Give the extent of all uninfected red blood cells.
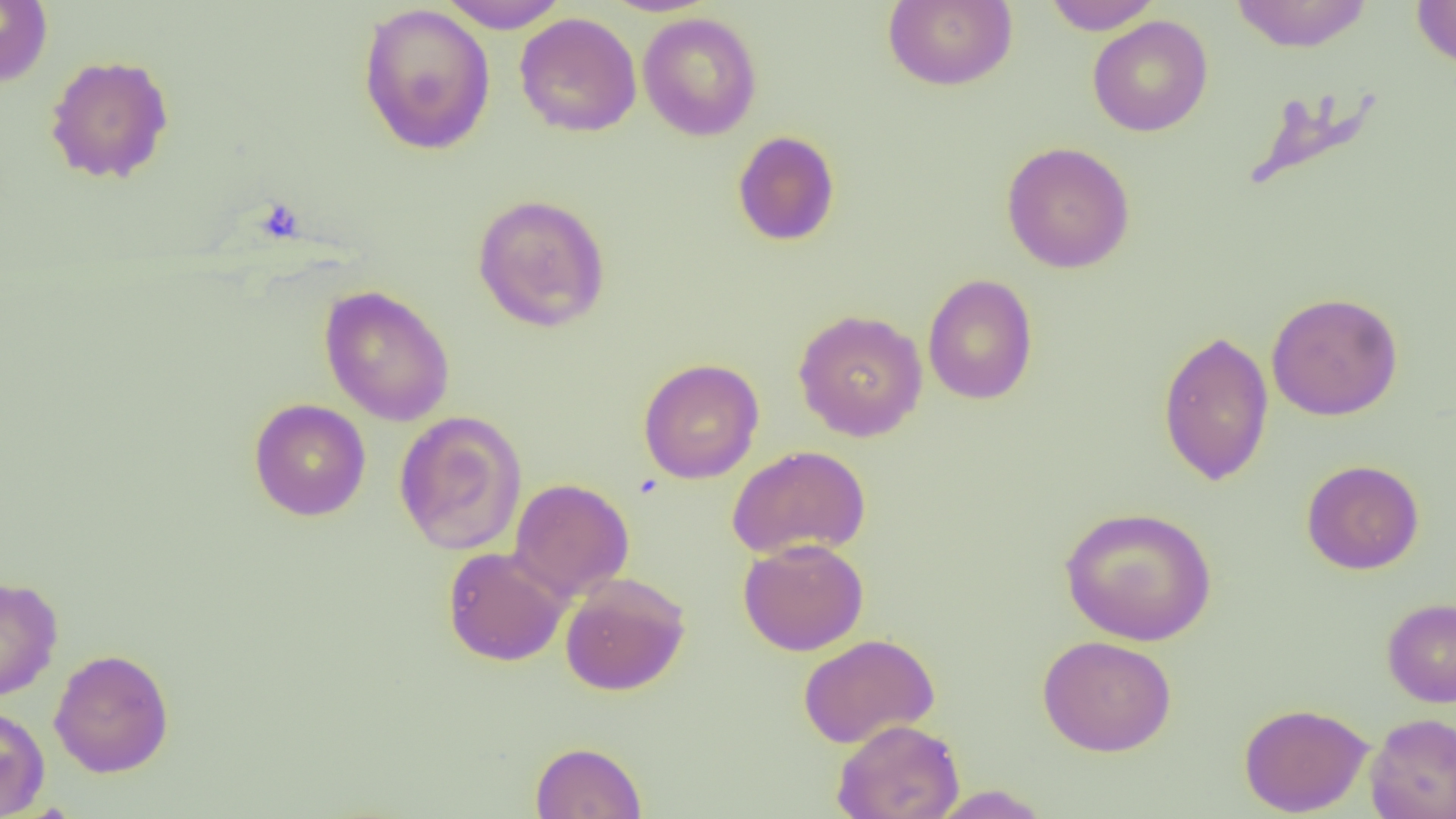
Approximate bounding boxes as [x1, y1, x2, y2] in pixels.
Uninfected red blood cells: [436, 0, 571, 33], [883, 0, 1017, 91], [1042, 0, 1162, 35], [1229, 0, 1374, 52], [1411, 0, 1456, 68], [0, 1, 53, 88], [357, 3, 496, 156], [637, 12, 762, 141], [514, 13, 642, 138], [1087, 15, 1214, 137], [45, 54, 174, 185], [1242, 86, 1385, 192], [732, 131, 840, 246], [1001, 141, 1135, 274], [472, 193, 611, 332], [922, 273, 1038, 405], [319, 285, 455, 426], [1266, 292, 1404, 421], [793, 308, 928, 442], [1157, 328, 1274, 487], [638, 358, 764, 484], [249, 398, 371, 521], [393, 410, 528, 556], [728, 445, 871, 561], [1301, 459, 1424, 574], [510, 478, 634, 600], [1060, 506, 1217, 646], [738, 538, 869, 656], [442, 546, 572, 666], [560, 573, 690, 696], [0, 575, 63, 702], [1382, 597, 1456, 708], [798, 633, 940, 749], [1038, 634, 1176, 757], [49, 648, 174, 778], [1239, 702, 1373, 817], [0, 704, 50, 817], [1364, 712, 1456, 819], [831, 718, 965, 819], [530, 741, 647, 819], [928, 785, 1053, 819].

Summary:
  - Platelet locations: [254, 198, 305, 244]
  - Slide-level diagnosis: no evidence of blood parasites
  - Magnification: 1000x
  - Image size: 1456×819 pixels
  - Modality: light microscopy
  - Field of view: one of a larger specimen
  - Preparation: thin blood film